Give the position of every leukocyte visible.
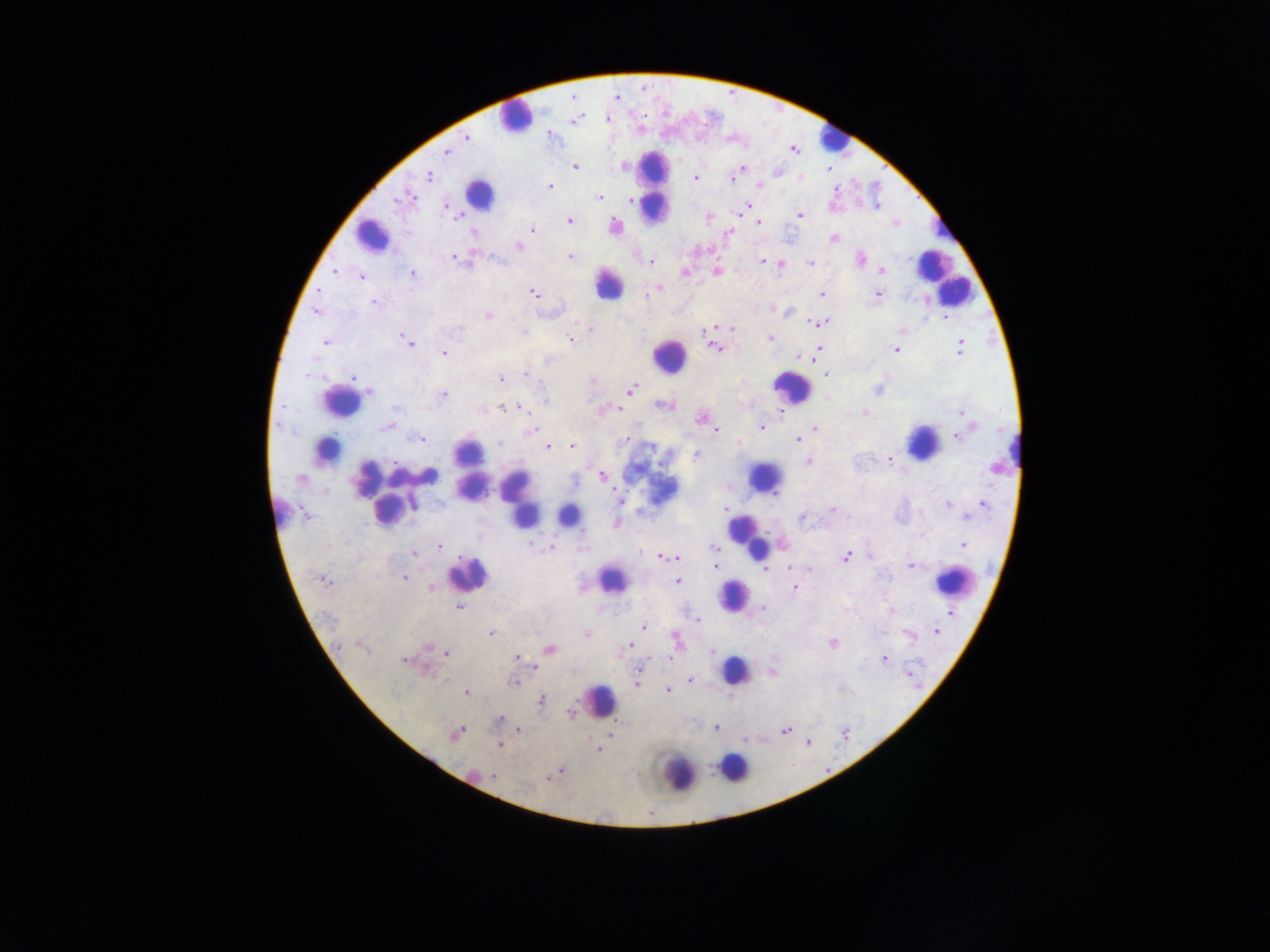

Approximate centers as x y in pixels.
Leukocytes: 515 116; 835 138; 654 185; 478 196; 372 237; 932 269; 943 277; 607 284; 952 292; 669 357; 790 388; 341 402; 923 442; 326 449; 1006 454; 469 467; 764 478; 471 486; 518 499; 387 501; 280 509; 524 513; 568 516; 747 537; 466 574; 611 580; 953 581; 734 595; 734 670; 599 701; 734 767; 676 772.

capture: mobile-phone photograph through a microscope
preparation: thick blood smear
country: Ghana
image_size: 1270×952 pixels
malaria_parasite_locations: 'approximate centers as x y in pixels: 573 96; 616 98; 606 117; 575 119; 549 132; 466 137; 792 149; 446 152; 575 167; 741 169; 829 170; 427 176; 695 178; 799 178; 550 185; 760 185; 406 196; 600 196; 629 201; 446 204; 747 206; 878 206; 744 211; 800 216; 708 217; 569 220; 758 221; 894 222; 615 227; 533 228; 728 233; 833 239; 519 246; 454 257; 570 257; 860 258; 651 261; 763 262; 810 263; 780 264; 882 270; 716 271; 334 272; 684 272; 412 273; 362 276; 661 288; 534 293; 822 295; 878 295; 374 302; 772 309; 316 311; 792 311; 487 316; 946 318; 822 322; 813 324; 724 327; 734 328; 590 329; 704 330; 901 331; 771 338; 570 339; 325 342; 408 342; 716 347; 960 347; 896 348; 819 349; 444 353; 797 355; 814 360; 525 375; 826 375; 353 377; 500 379; 878 388; 630 390; 367 391; 442 394; 544 399; 665 405; 501 407; 521 408; 601 408; 782 410; 960 412; 865 413; 700 417; 969 425; 389 426; 762 427; 815 429; 715 430; 530 431; 421 438; 957 438; 797 439; 624 440; 739 442; 499 443; 572 445; 548 446; 694 455; 889 457; 807 462; 602 476; 620 501; 981 503; 948 504; 726 510; 832 510; 801 517; 965 518; 614 525; 962 544; 439 546; 550 547; 713 548; 413 552; 661 556; 668 556; 847 556; 870 556; 678 557; 716 566; 790 566; 909 566; 767 569; 404 578; 324 580; 676 581; 432 587; 795 588; 458 606; 763 607; 891 612; 950 613; 697 620; 644 627; 934 631; 491 632; 585 634; 909 634; 831 642; 676 643; 628 645; 361 647; 548 649; 447 653; 518 657; 885 659; 407 661; 535 667; 640 669; 772 670; 690 679; 514 682; 637 683; 667 690; 465 692; 541 699; 572 713; 498 720; 716 728; 519 729; 785 730; 610 732; 455 733; 499 745; 598 748; 557 771; 494 776'
field_of_view: single